Give the extent of all Plasmodium falciparum-infected red blood cells.
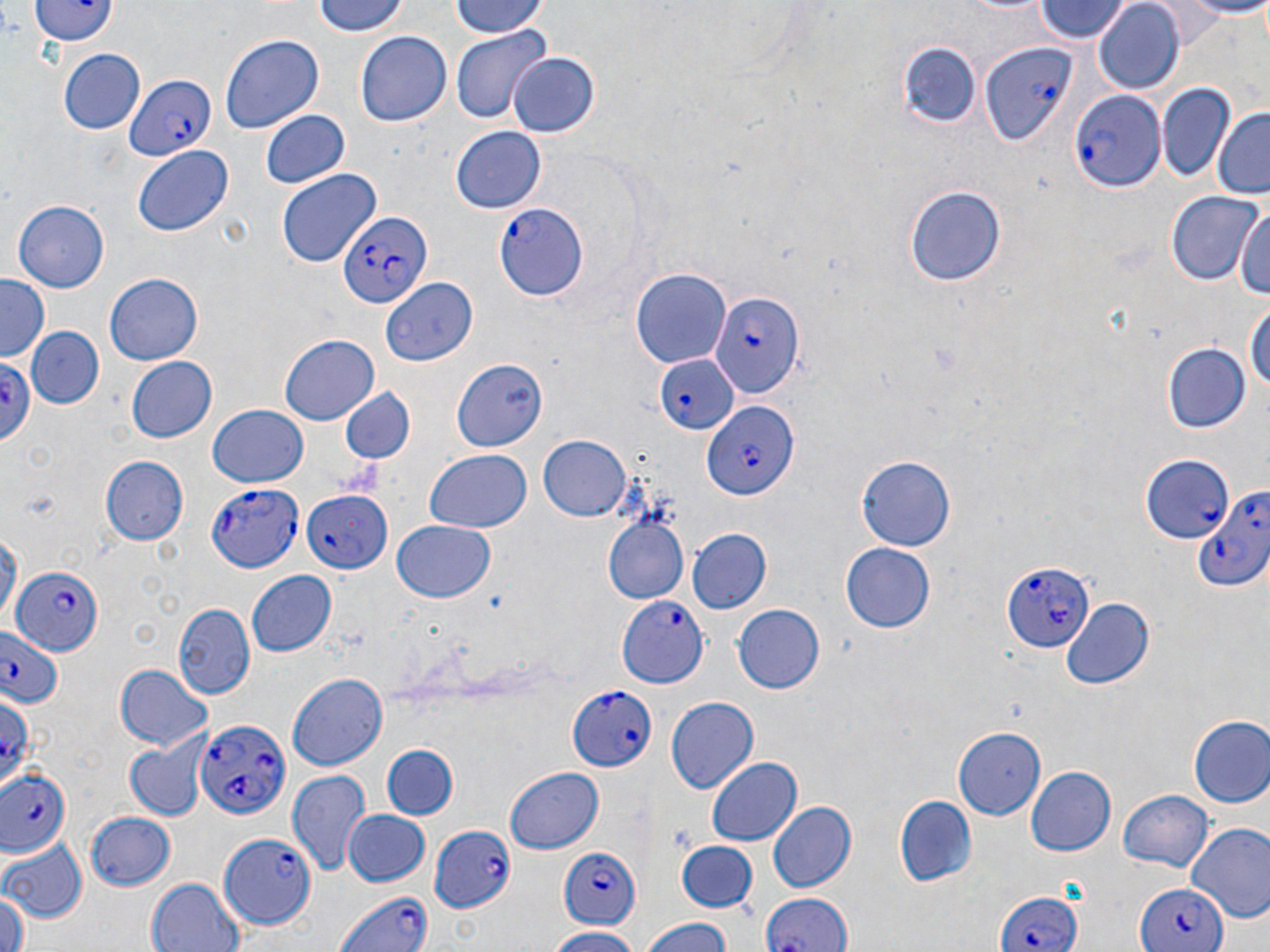
Approximate bounding boxes as (x1,y1)-(x2,y2) corner pairs in pixels.
Plasmodium falciparum-infected red blood cells (subset): (980,43)-(1078,144), (122,73)-(215,163), (1068,88)-(1166,193), (494,201)-(590,299), (337,213)-(430,310), (708,292)-(801,399), (657,353)-(738,435), (0,358)-(36,443), (702,403)-(800,502), (1143,452)-(1232,543), (205,480)-(305,572), (1194,486)-(1269,593), (301,490)-(392,572), (1002,558)-(1097,654), (10,566)-(102,658), (0,623)-(64,706), (565,685)-(656,773), (198,715)-(289,819), (3,769)-(72,856), (428,825)-(516,912), (217,831)-(315,927), (557,846)-(640,930), (1130,881)-(1228,952), (994,888)-(1080,952), (330,889)-(437,952), (757,890)-(851,952).

Summary:
  - Uninfected red blood cell locations (subset): (34,0)-(115,47), (314,0)-(414,39), (449,0)-(551,39), (1091,0)-(1185,92), (1177,0)-(1270,17), (1031,1)-(1132,43), (356,27)-(451,125), (451,29)-(548,122), (220,33)-(324,135), (901,40)-(981,129), (58,49)-(144,135), (508,50)-(599,136), (247,55)-(342,181), (1157,81)-(1236,183), (1211,108)-(1270,200), (260,109)-(349,191), (452,127)-(545,213), (132,145)-(236,236), (276,169)-(379,268), (903,183)-(1007,288), (1166,190)-(1263,283), (11,199)-(109,293), (1232,199)-(1269,303), (631,270)-(730,367), (106,274)-(202,363), (1,275)-(52,362), (1245,296)-(1270,403), (28,326)-(102,407), (280,334)-(378,422), (1163,343)-(1251,434), (126,356)-(216,443), (454,356)-(548,450), (337,387)-(416,466), (207,404)-(310,488), (539,436)-(631,522), (423,450)-(533,533), (103,455)-(188,546), (858,455)-(958,550), (602,517)-(688,606), (391,521)-(496,603), (686,530)-(770,615), (841,544)-(936,632), (245,569)-(337,657), (1060,599)-(1155,692), (172,603)-(255,700), (732,605)-(824,692), (115,665)-(212,753), (289,671)-(388,770), (665,698)-(756,793), (1188,716)-(1270,808), (952,728)-(1047,816), (124,740)-(206,820), (379,745)-(459,821), (708,759)-(801,845), (1025,763)-(1116,856), (505,767)-(603,853), (285,769)-(371,878), (1118,790)-(1214,872), (894,796)-(975,886), (768,801)-(855,894), (342,810)-(432,887), (84,811)-(178,890), (0,840)-(86,924), (677,842)-(759,911), (145,878)-(242,952), (0,888)-(27,952), (640,918)-(737,952), (544,928)-(644,952)
  - Slide-level diagnosis: Plasmodium falciparum
  - Image size: 1270×952 pixels
  - Stain: May-Grünwald-Giemsa
  - Field of view: one of a larger specimen
  - Modality: optical microscopy
  - Magnification: 1000x
  - Preparation: thin blood film